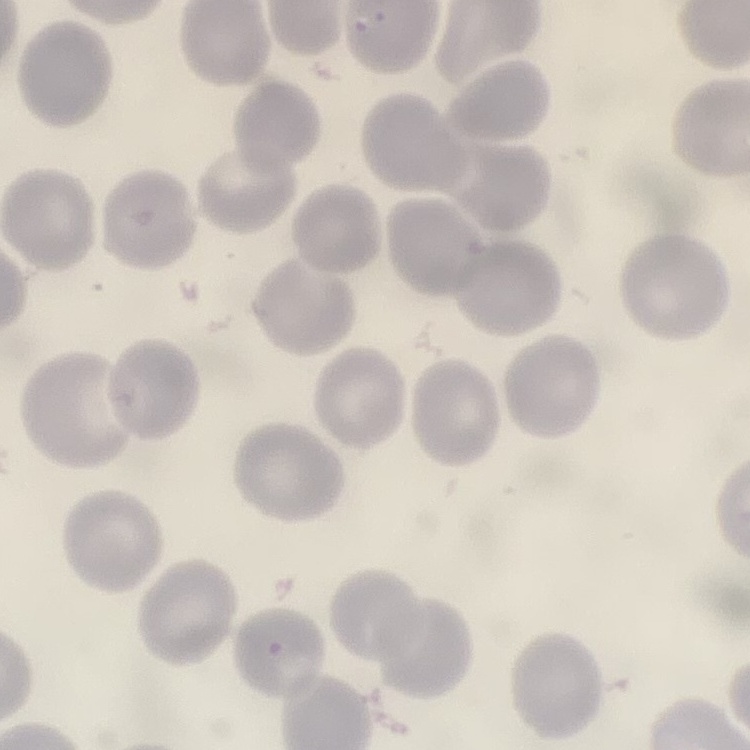

erythrocyte morphology = no rouleaux formation
stain = Field's or Giemsa
preparation = thin blood smear
image type = one tile cut from a larger photomicrograph